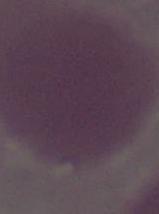

Photomicrograph. Captured at 1000x magnification. A red blood cell is seen.